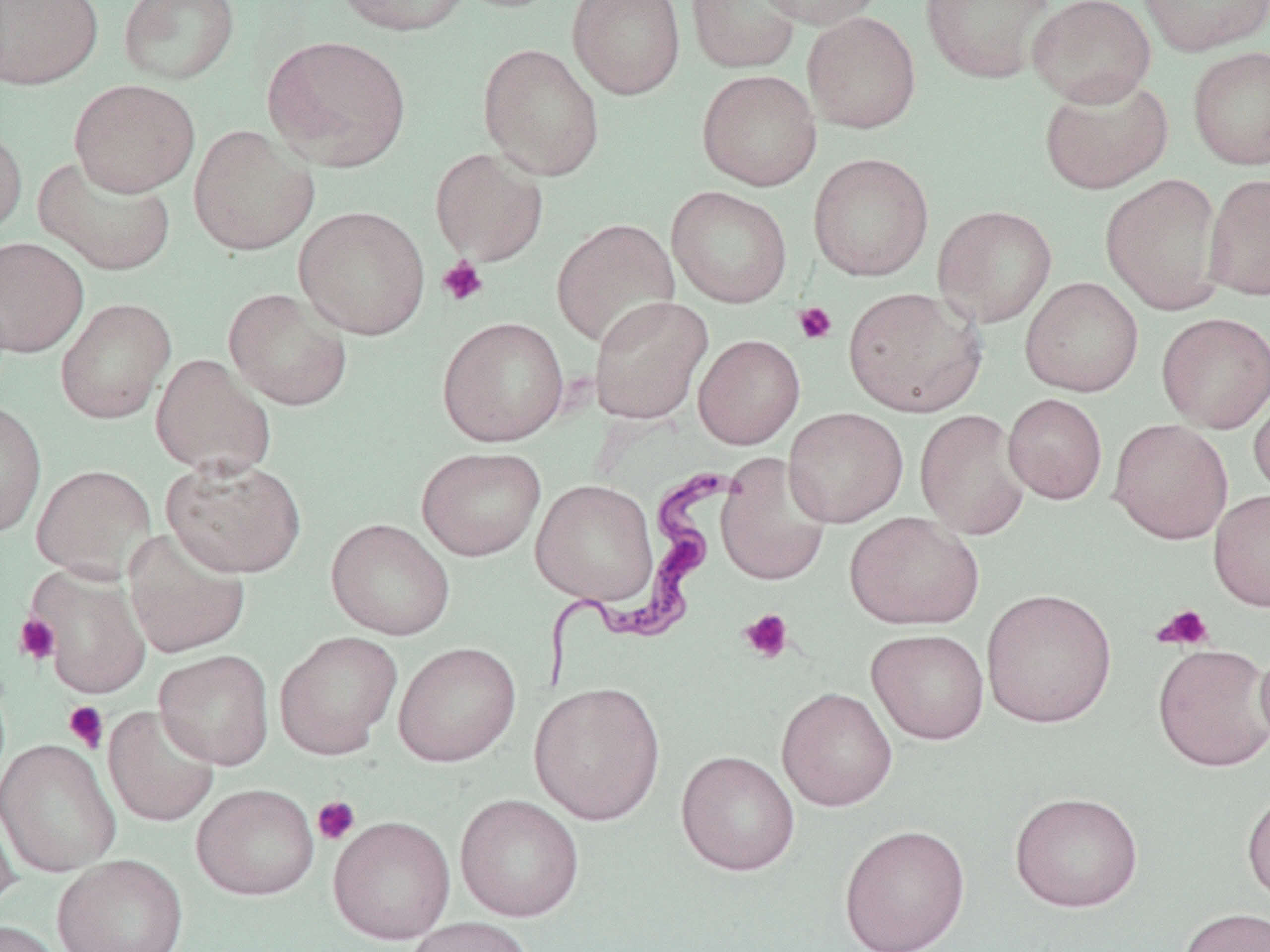
{
  "slide_level_diagnosis": "Trypanosoma brucei",
  "uninfected_red_blood_cell_locations_subset": "approximate bounding boxes as (x1,y1)-(x2,y2) corner pairs in pixels: (0,0)-(104,91), (117,0)-(240,85), (335,0)-(472,37), (450,0)-(568,14), (566,0)-(686,100), (685,0)-(801,74), (754,0)-(886,30), (920,0)-(1055,84), (1026,0)-(1157,107), (1136,0)-(1270,57), (802,12)-(921,134), (262,35)-(412,172), (477,43)-(605,180), (1187,46)-(1270,169), (696,69)-(822,190), (1038,74)-(1173,195), (68,78)-(200,197), (0,121)-(27,241), (188,124)-(319,256), (430,148)-(548,266), (808,153)-(934,280), (34,154)-(176,276), (1100,172)-(1227,315), (1202,172)-(1270,302), (666,186)-(793,308), (294,205)-(431,340), (932,205)-(1057,327), (550,218)-(681,349), (0,236)-(89,357), (1020,277)-(1143,397), (223,286)-(352,411), (843,286)-(986,417), (588,296)-(713,424), (55,297)-(176,424), (1156,312)-(1270,433), (437,316)-(569,447), (693,334)-(804,450), (150,353)-(276,479), (1250,388)-(1270,501), (1003,393)-(1108,504), (0,400)-(47,539), (783,407)-(908,527), (914,409)-(1030,540), (1108,418)-(1233,544), (416,446)-(546,561), (715,454)-(832,586), (162,455)-(307,578), (31,464)-(157,582), (530,479)-(657,604), (845,512)-(984,630), (325,518)-(455,640), (123,527)-(251,659), (26,564)-(151,699), (981,588)-(1117,728), (867,629)-(989,744), (274,631)-(402,759), (1255,641)-(1270,753), (393,642)-(521,766), (1153,643)-(1270,772), (154,649)-(274,769), (529,681)-(666,825), (776,687)-(898,811), (103,704)-(220,828), (0,739)-(121,877), (676,750)-(800,876), (191,783)-(320,901), (1241,785)-(1270,907), (1009,790)-(1144,912), (454,794)-(585,922), (0,801)-(21,916), (328,816)-(456,944), (838,824)-(970,952), (53,853)-(189,952), (1177,906)-(1269,952), (403,917)-(536,952), (0,920)-(64,952)",
  "trypanosoma_brucei_locations": "approximate bounding boxes as (x1,y1)-(x2,y2) corner pairs in pixels: (537,461)-(735,694)",
  "magnification": "1000x",
  "field_of_view": "one of a larger specimen",
  "modality": "optical microscopy",
  "preparation": "thin blood smear",
  "stain": "May-Grünwald-Giemsa",
  "platelet_locations_subset": "approximate bounding boxes as (x1,y1)-(x2,y2) corner pairs in pixels: (437,257)-(489,307), (793,301)-(837,345), (1153,603)-(1215,651), (739,608)-(794,664), (13,613)-(61,666), (63,701)-(109,753), (312,796)-(359,845)",
  "image_size": "1270×952 pixels"
}